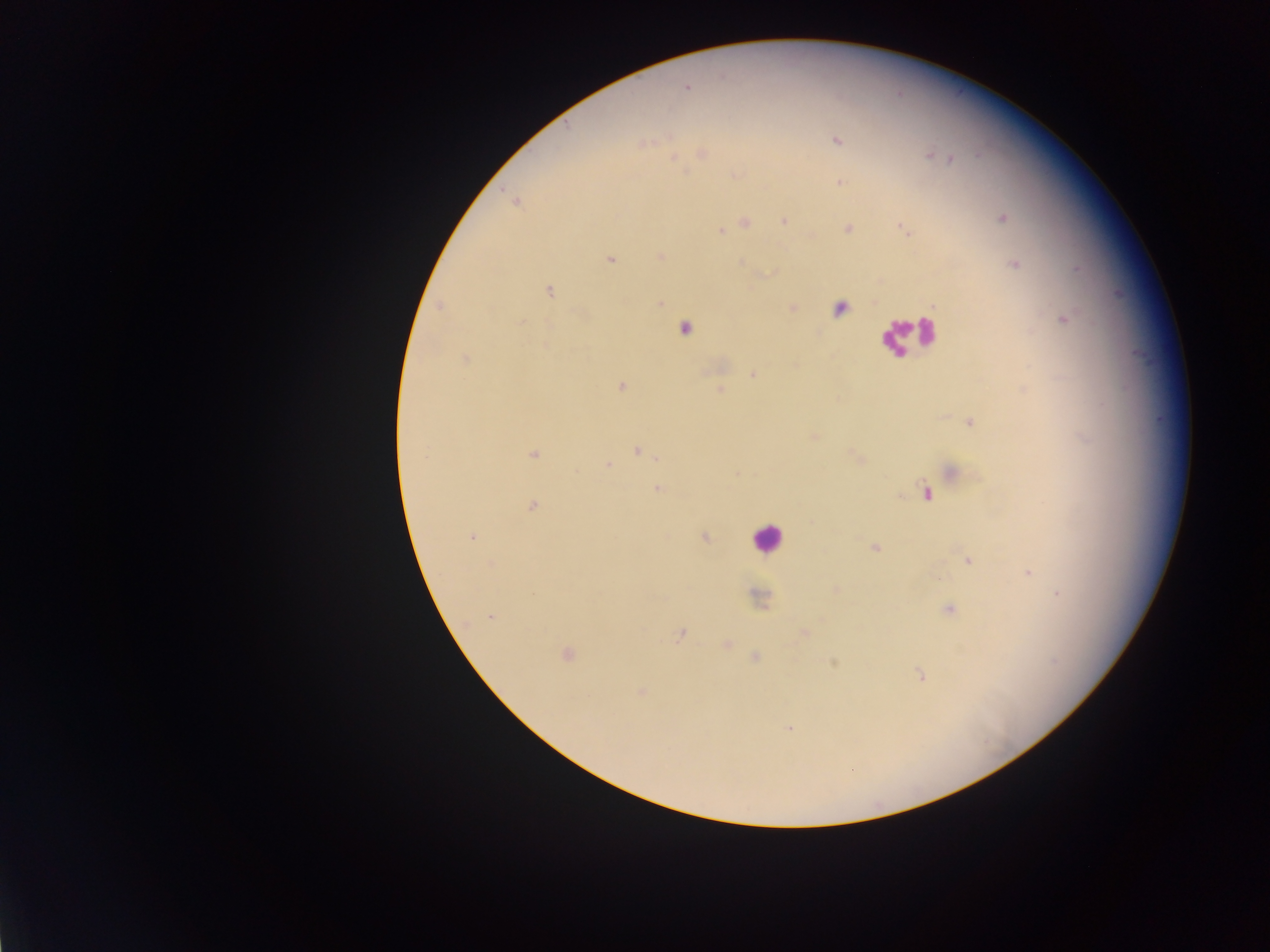

Approximate centers as x y in pixels. Plasmodium parasite locations: 686 87; 837 141; 703 154; 930 156; 950 159; 840 183; 516 201; 1003 218; 784 221; 746 224; 847 229; 904 229; 721 231; 661 256; 610 260; 741 263; 1015 264; 549 291; 661 303; 439 306; 793 308; 1063 320; 520 323; 465 358; 753 375; 622 386; 719 390; 970 422; 814 436; 638 451; 534 454; 856 457; 608 465; 953 472; 657 489; 926 494; 532 506; 471 537; 704 537; 875 548; 968 560; 491 564; 1028 572; 836 589; 1059 593; 758 599; 949 610; 491 617; 804 634; 680 635; 727 644; 566 654; 755 657; 833 663; 920 675; 641 692; 789 728. Leukocyte locations: 837 309; 687 329; 906 334; 765 538. Thick blood film. Collected in Ghana. Image is 1270×952 pixels. One field of view. Photographed through a microscope with a mobile-phone camera.